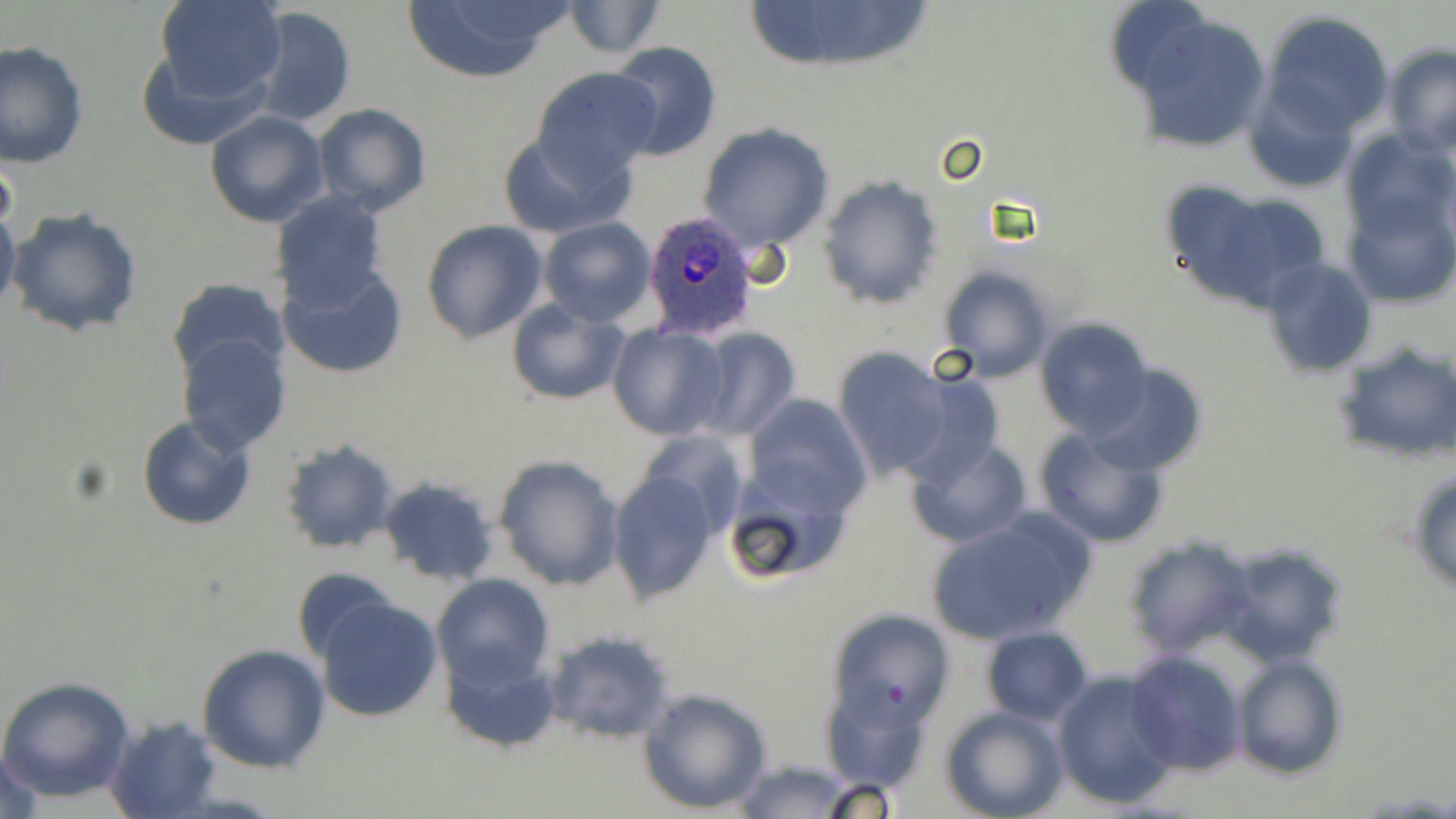
{
  "slide_level_diagnosis": "Plasmodium ovale",
  "preparation": "thin blood smear",
  "stain": "May-Grünwald-Giemsa",
  "image_size": "1456×819 pixels",
  "magnification": "1000x",
  "field_of_view": "one of a larger specimen",
  "plasmodium_ovale_infected_red_blood_cell_locations": "approximate bounding boxes as named x1/y1/x2/y2 corners in pixels: (x1=644, y1=212, x2=757, y2=339)",
  "modality": "optical microscopy",
  "uninfected_red_blood_cell_locations": "approximate bounding boxes as named x1/y1/x2/y2 corners in pixels: (x1=154, y1=0, x2=288, y2=106), (x1=401, y1=0, x2=571, y2=83), (x1=747, y1=0, x2=936, y2=73), (x1=1106, y1=0, x2=1218, y2=97), (x1=564, y1=1, x2=665, y2=58), (x1=247, y1=7, x2=356, y2=128), (x1=1127, y1=9, x2=1273, y2=155), (x1=1264, y1=12, x2=1394, y2=136), (x1=607, y1=40, x2=722, y2=162), (x1=0, y1=42, x2=88, y2=168), (x1=1383, y1=43, x2=1456, y2=157), (x1=138, y1=46, x2=268, y2=148), (x1=531, y1=67, x2=661, y2=182), (x1=1242, y1=83, x2=1358, y2=196), (x1=312, y1=104, x2=432, y2=217), (x1=204, y1=109, x2=328, y2=227), (x1=697, y1=122, x2=834, y2=251), (x1=498, y1=129, x2=626, y2=238), (x1=1340, y1=129, x2=1455, y2=248), (x1=818, y1=174, x2=944, y2=308), (x1=1160, y1=181, x2=1329, y2=310), (x1=1344, y1=186, x2=1455, y2=312), (x1=269, y1=190, x2=391, y2=310), (x1=0, y1=199, x2=20, y2=321), (x1=6, y1=208, x2=143, y2=338), (x1=538, y1=218, x2=656, y2=327), (x1=421, y1=220, x2=549, y2=343), (x1=1260, y1=257, x2=1378, y2=376), (x1=280, y1=264, x2=407, y2=379), (x1=935, y1=265, x2=1057, y2=384), (x1=172, y1=276, x2=289, y2=378), (x1=505, y1=298, x2=632, y2=407), (x1=1036, y1=318, x2=1154, y2=438), (x1=607, y1=323, x2=727, y2=440), (x1=689, y1=328, x2=800, y2=441), (x1=175, y1=332, x2=291, y2=456), (x1=1333, y1=340, x2=1455, y2=463), (x1=834, y1=346, x2=952, y2=479), (x1=1087, y1=363, x2=1206, y2=476), (x1=901, y1=372, x2=1005, y2=486), (x1=744, y1=393, x2=870, y2=519), (x1=137, y1=414, x2=255, y2=530), (x1=1034, y1=425, x2=1172, y2=547), (x1=632, y1=430, x2=748, y2=541), (x1=905, y1=436, x2=1031, y2=548), (x1=279, y1=437, x2=401, y2=554), (x1=491, y1=453, x2=625, y2=591), (x1=607, y1=468, x2=717, y2=602), (x1=1408, y1=468, x2=1456, y2=596), (x1=722, y1=470, x2=854, y2=588), (x1=374, y1=476, x2=502, y2=586), (x1=927, y1=506, x2=1098, y2=643), (x1=1122, y1=535, x2=1258, y2=657), (x1=1215, y1=542, x2=1349, y2=668), (x1=294, y1=567, x2=403, y2=668), (x1=431, y1=574, x2=554, y2=687), (x1=311, y1=593, x2=445, y2=723), (x1=828, y1=610, x2=953, y2=731), (x1=981, y1=627, x2=1093, y2=723), (x1=541, y1=629, x2=678, y2=744), (x1=196, y1=642, x2=331, y2=773), (x1=440, y1=644, x2=562, y2=754), (x1=1125, y1=650, x2=1248, y2=776), (x1=1231, y1=652, x2=1346, y2=780), (x1=1052, y1=670, x2=1179, y2=808), (x1=0, y1=675, x2=137, y2=804), (x1=638, y1=686, x2=772, y2=813), (x1=941, y1=706, x2=1067, y2=819), (x1=101, y1=714, x2=221, y2=819), (x1=0, y1=747, x2=48, y2=819), (x1=727, y1=759, x2=862, y2=818)"
}